Locate every Plasmodium parasite.
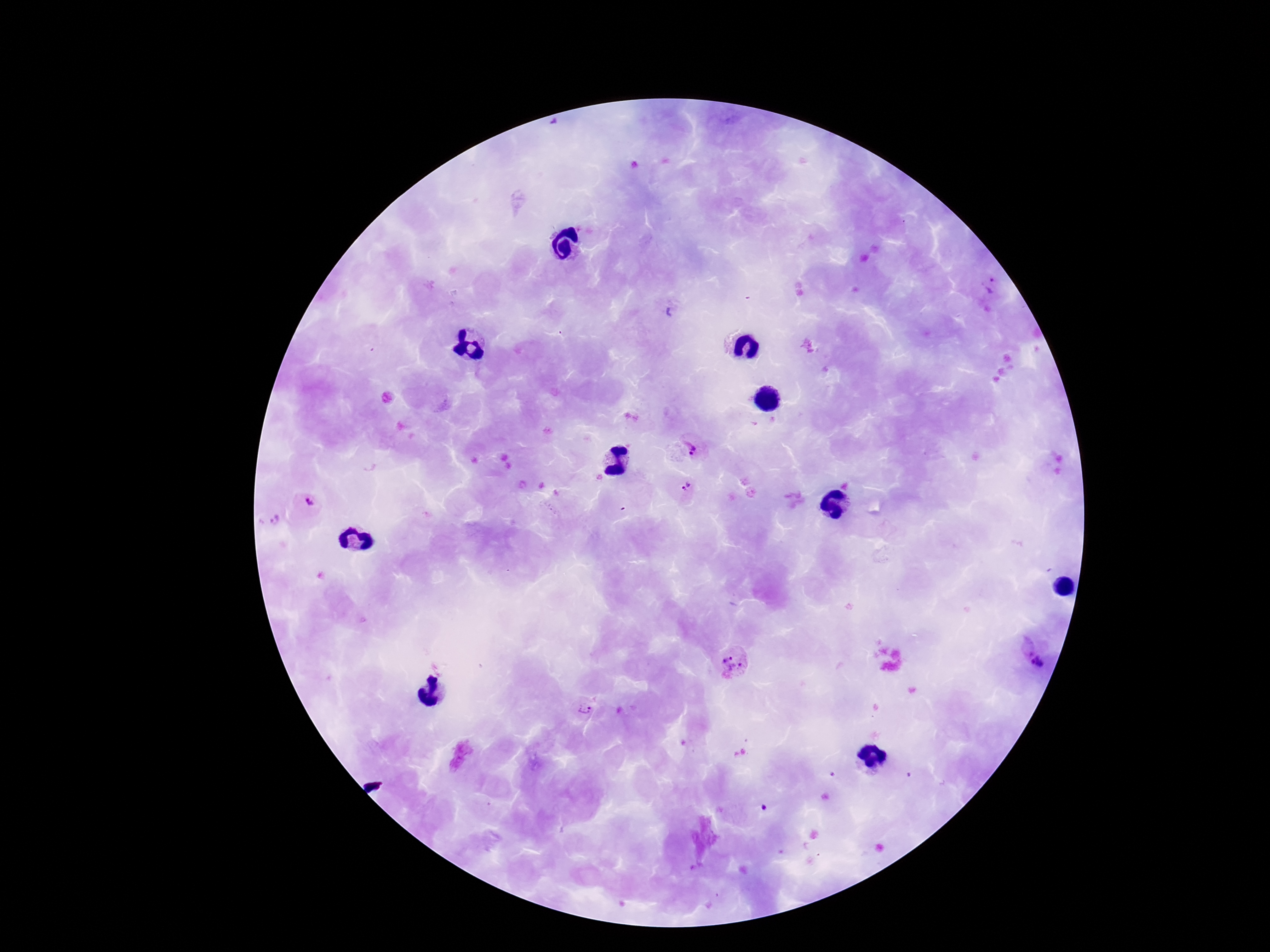

Approximate object centers, in pixels from the top-left corner.
Plasmodium parasites: (x=987, y=287), (x=696, y=448), (x=685, y=487), (x=306, y=506), (x=268, y=520), (x=1024, y=645), (x=731, y=664), (x=1043, y=666), (x=583, y=710).

Summary:
  - Image size: 1270×952 pixels
  - Preparation: thick peripheral-blood smear
  - Magnification: 100x
  - Capture: smartphone camera through the microscope eyepiece
  - Patient malaria status: positive
  - Field of view: single
  - Stain: Giemsa